Assess this cell for malaria.
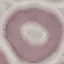
It is uninfected.

Summary:
  - Stain: Giemsa
  - Capture: smartphone camera at the microscope eyepiece
  - Preparation: thin blood smear
  - Image type: automatically extracted cell patch, resized to 64 × 64 pixels